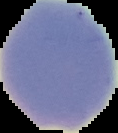
Summary:
  - Image size: 118×133 pixels
  - Image type: cell region segmented out of the field of view; surrounding area masked to black
  - Result: no Plasmodium parasites seen
  - Preparation: thin blood film